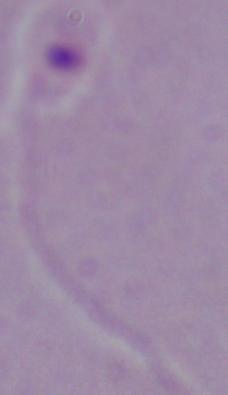
1000x magnification. Photomicrograph. A Leishmania parasite is shown.